Give the position of every Plasmodium parasite visible.
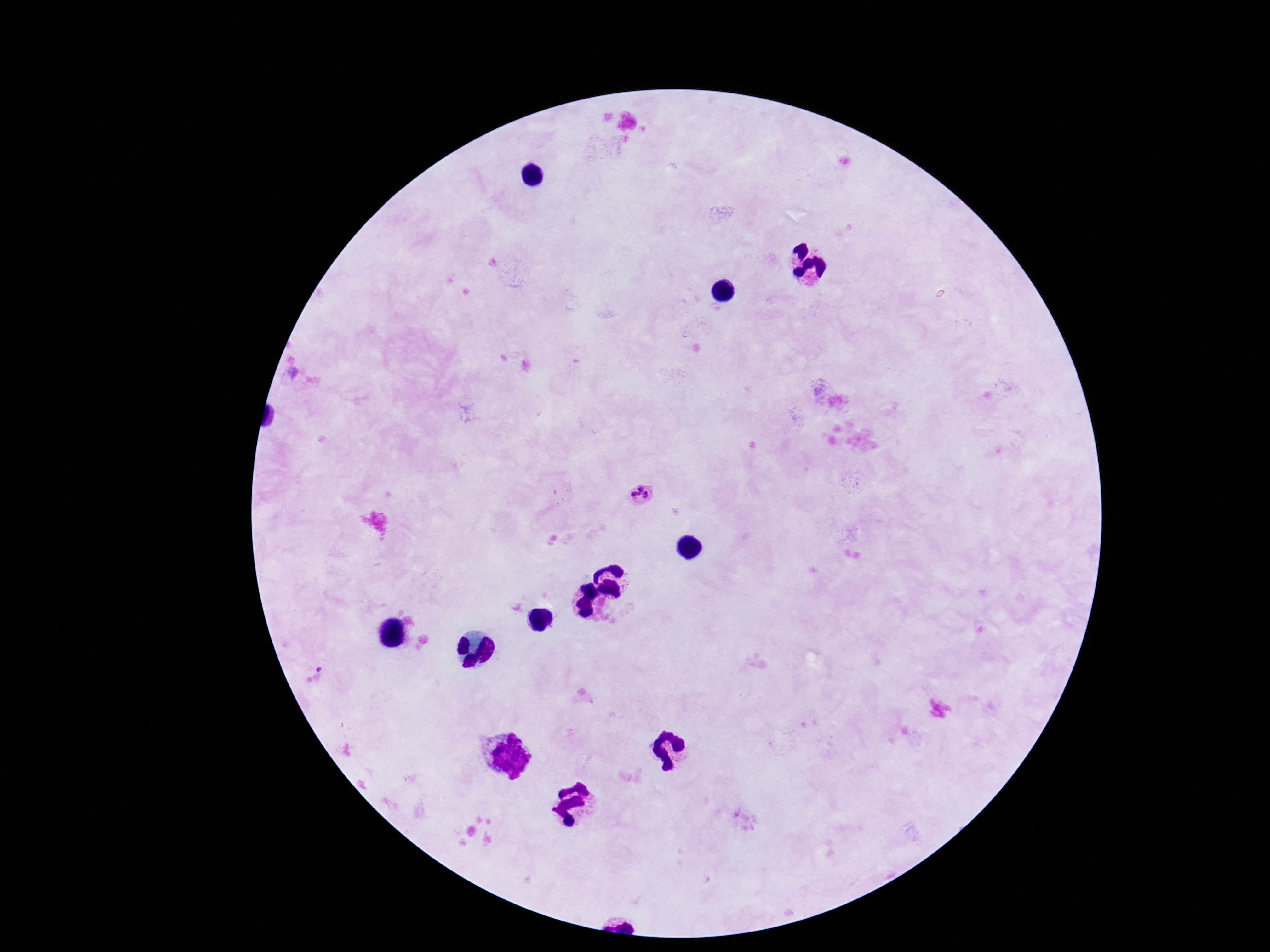

Approximate centers as {x, y} in pixels.
Plasmodium parasites: {642, 496}.

preparation: thick blood smear
magnification: 100x
patient_malaria_status: infected
image_size: 1270×952 pixels
field_of_view: one from this slide
stain: Giemsa
capture: smartphone camera through the microscope eyepiece